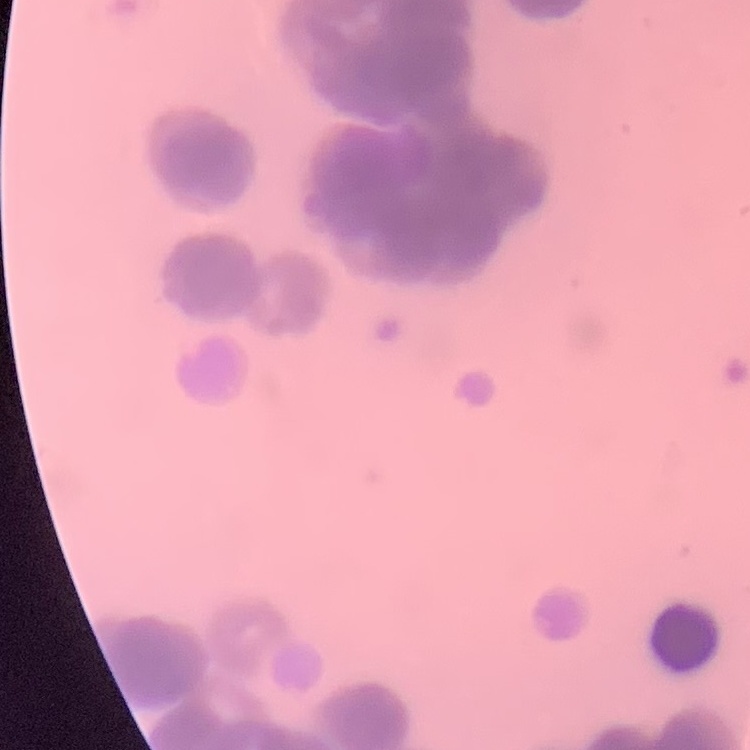

erythrocyte morphology = rouleaux formation
image type = square crop of a larger photomicrograph
stain = Field's or Giemsa
preparation = thin blood smear